Look for Plasmodium parasites.
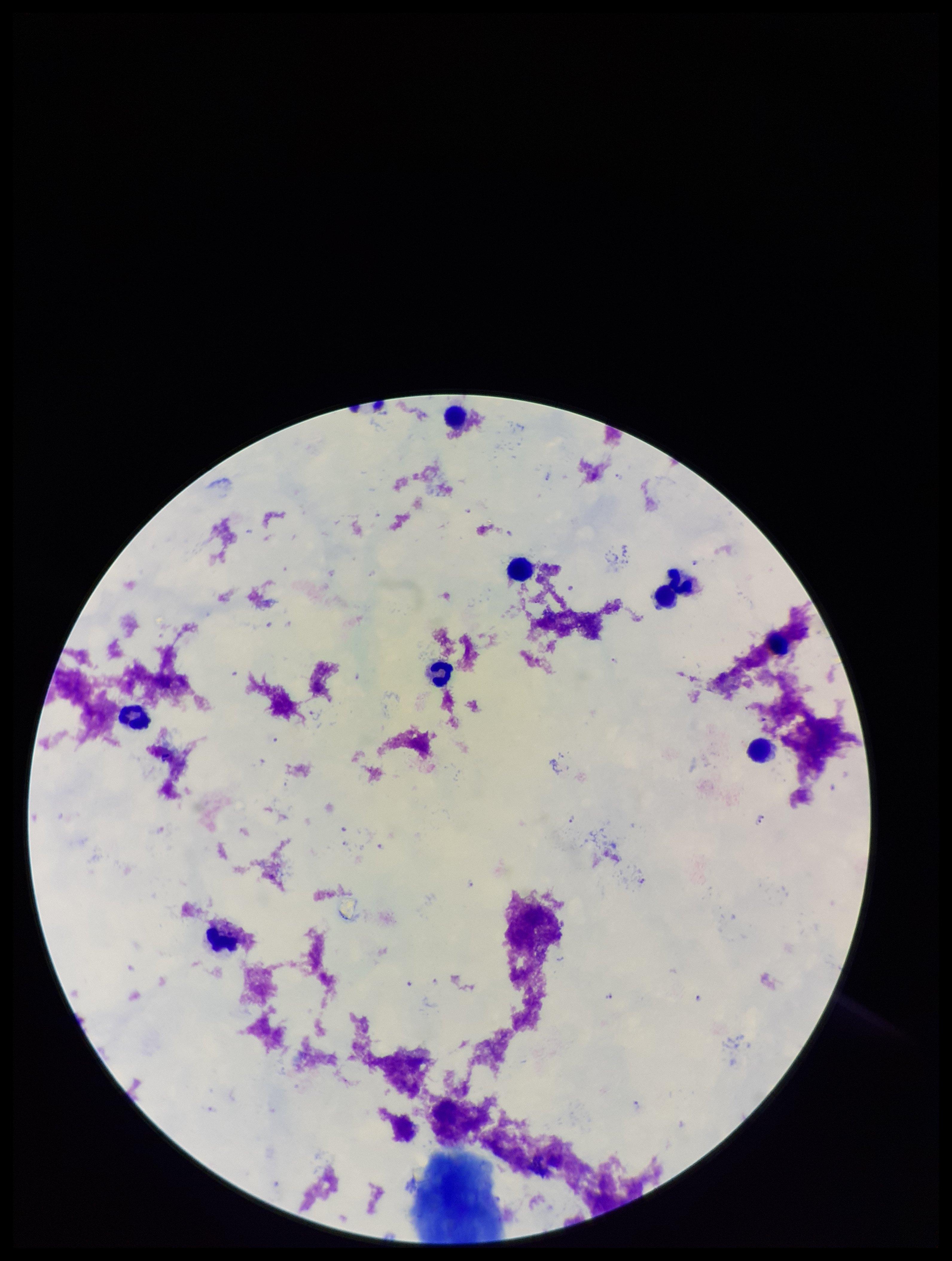
Identified.

Summary:
  - Parasite count: 8
  - Field of view: one from this slide
  - Leukocyte count: 9
  - Capture: smartphone photograph through the microscope eyepiece
  - Patient malaria status: infected
  - Preparation: thick
  - Stain: Giemsa
  - Species reported for this patient: Plasmodium falciparum
  - Image size: 952×1261 pixels